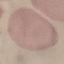

Summary:
  - Result: no malaria parasites detected
  - Preparation: thin blood smear
  - Capture: smartphone through the microscope eyepiece
  - Image type: cell patch, automatically extracted from a larger field of view and resized to 64 × 64 pixels
  - Stain: Giemsa